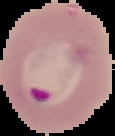

Summary:
  - Result: Plasmodium parasites identified
  - Image type: segmented cell region with the area outside set to black
  - Image size: 115×136 pixels
  - Preparation: thin blood smear